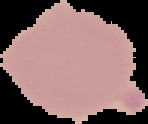

Segmented cell region on a black background. From a thin blood smear. Malaria status: uninfected. Image is 148×124 pixels.